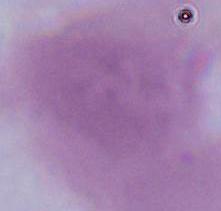

identification = red blood cell
magnification = 1000x
modality = photomicrograph